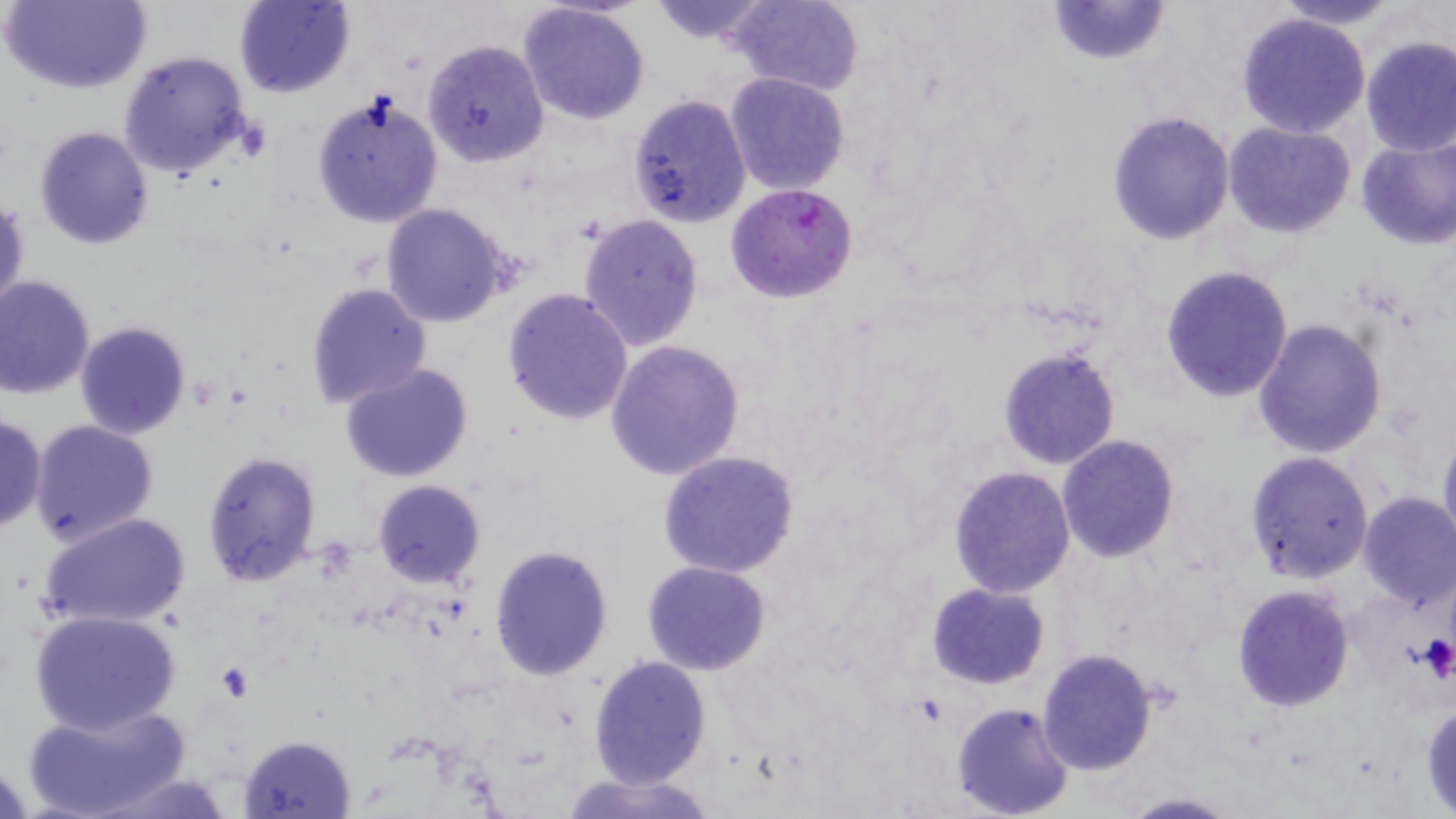
Summary:
  - Coordinate format: approximate bounding boxes as (x1, y1, x2, y2) in pixels
  - Platelet locations: (1419, 634, 1455, 683)
  - Uninfected red blood cell locations: (4, 0, 151, 94), (233, 0, 355, 100), (646, 0, 774, 46), (725, 0, 864, 96), (1045, 0, 1172, 66), (1274, 0, 1401, 29), (516, 3, 650, 126), (1234, 12, 1370, 139), (1360, 36, 1456, 157), (421, 40, 549, 168), (116, 50, 254, 183), (725, 72, 850, 195), (309, 91, 444, 229), (626, 94, 751, 227), (1106, 111, 1234, 245), (1223, 122, 1355, 239), (33, 126, 154, 249), (1354, 133, 1456, 250), (0, 196, 28, 318), (378, 203, 515, 329), (577, 213, 704, 352), (1160, 265, 1293, 402), (0, 275, 96, 398), (304, 281, 433, 411), (501, 288, 634, 426), (1251, 318, 1388, 458), (73, 321, 192, 440), (605, 341, 745, 480), (998, 345, 1121, 469), (340, 362, 475, 483), (0, 413, 47, 534), (28, 418, 159, 547), (1438, 427, 1456, 555), (1057, 435, 1180, 562), (201, 451, 322, 587), (658, 451, 803, 578), (1245, 453, 1373, 582), (949, 465, 1076, 596), (371, 479, 485, 588), (1356, 494, 1456, 611), (38, 511, 193, 631), (489, 545, 613, 682), (642, 561, 770, 676), (926, 581, 1051, 690), (1231, 585, 1353, 712), (29, 608, 184, 736), (1036, 649, 1160, 775), (589, 656, 710, 788), (20, 700, 193, 819), (951, 701, 1076, 819), (1422, 701, 1456, 814), (237, 733, 358, 817), (559, 771, 719, 819), (1113, 791, 1242, 819)
  - Plasmodium falciparum-infected red blood cell locations: (725, 182, 859, 302)
  - Slide-level diagnosis: Plasmodium falciparum
  - Stain: May-Grünwald-Giemsa
  - Magnification: 1000x
  - Field of view: one of a larger specimen
  - Image size: 1456×819 pixels
  - Modality: optical microscopy
  - Preparation: thin blood film